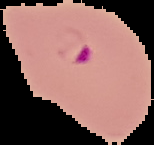 Image is 154×145 pixels. From a thin blood film. Cell region segmented out of the field of view; the surrounding area is masked to black. Result: Plasmodium parasites detected.